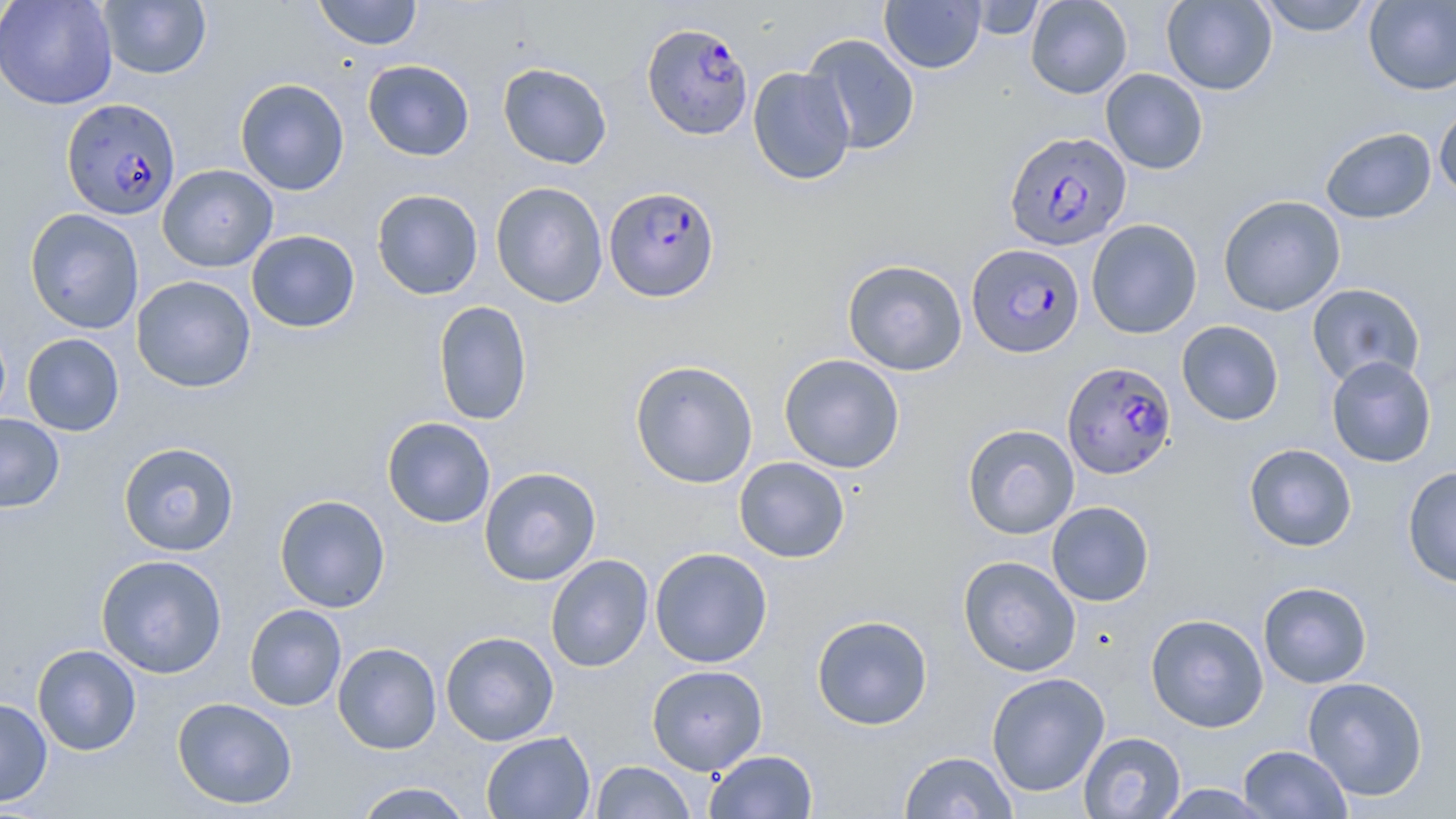

plasmodium_falciparum_infected_red_blood_cell_locations: 'approximate bounding boxes as (x1, y1, x2, y2) in pixels: (642, 21, 752, 139), (61, 97, 181, 221), (1004, 131, 1131, 251), (604, 185, 720, 302), (971, 242, 1089, 357), (1062, 361, 1177, 480)'
slide_level_diagnosis: Plasmodium falciparum
uninfected_red_blood_cell_locations: 'approximate bounding boxes as (x1, y1, x2, y2) in pixels: (0, 0, 118, 110), (312, 0, 423, 50), (879, 0, 986, 73), (1025, 0, 1132, 99), (1161, 0, 1277, 95), (1255, 0, 1376, 36), (98, 1, 211, 79), (966, 1, 1046, 40), (1363, 1, 1456, 95), (802, 34, 920, 155), (362, 60, 475, 161), (497, 63, 612, 169), (747, 66, 856, 185), (1100, 68, 1207, 174), (234, 78, 349, 196), (1434, 102, 1456, 202), (1320, 126, 1437, 224), (157, 164, 278, 272), (490, 181, 608, 308), (371, 189, 484, 299), (1218, 195, 1346, 316), (24, 208, 144, 334), (1086, 218, 1203, 339), (246, 229, 360, 333), (842, 259, 968, 376), (131, 275, 256, 392), (1306, 283, 1426, 388), (433, 301, 532, 426), (1176, 320, 1284, 426), (21, 333, 124, 436), (779, 354, 905, 473), (1326, 355, 1437, 468), (630, 360, 759, 489), (0, 414, 65, 512), (381, 416, 496, 528), (962, 424, 1079, 539), (118, 441, 240, 557), (1243, 443, 1357, 551), (734, 456, 849, 563), (479, 466, 602, 586), (1402, 466, 1456, 588), (274, 494, 390, 613), (1046, 501, 1154, 606), (649, 547, 773, 668), (96, 554, 228, 678), (545, 554, 654, 672), (958, 555, 1081, 677), (1257, 581, 1373, 689), (243, 604, 347, 711), (1145, 613, 1269, 733), (811, 614, 933, 730), (440, 631, 559, 745), (332, 642, 442, 754), (32, 644, 141, 756), (646, 664, 768, 775), (986, 672, 1110, 797), (1302, 676, 1429, 802), (0, 697, 52, 807), (172, 697, 297, 809), (480, 731, 595, 818), (1078, 731, 1186, 818), (1238, 744, 1352, 818), (704, 749, 818, 818), (899, 751, 1018, 818), (590, 761, 696, 818), (352, 782, 475, 818), (1153, 783, 1277, 818)'
field_of_view: single
magnification: 1000x
modality: light microscopy
preparation: thin blood film
image_size: 1456×819 pixels
stain: May-Grünwald-Giemsa